State which parasite is depicted.
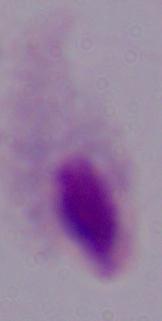

A trichomonad.

Photomicrograph. Captured at 1000x magnification.